Locate every blood parasite and identify its species.
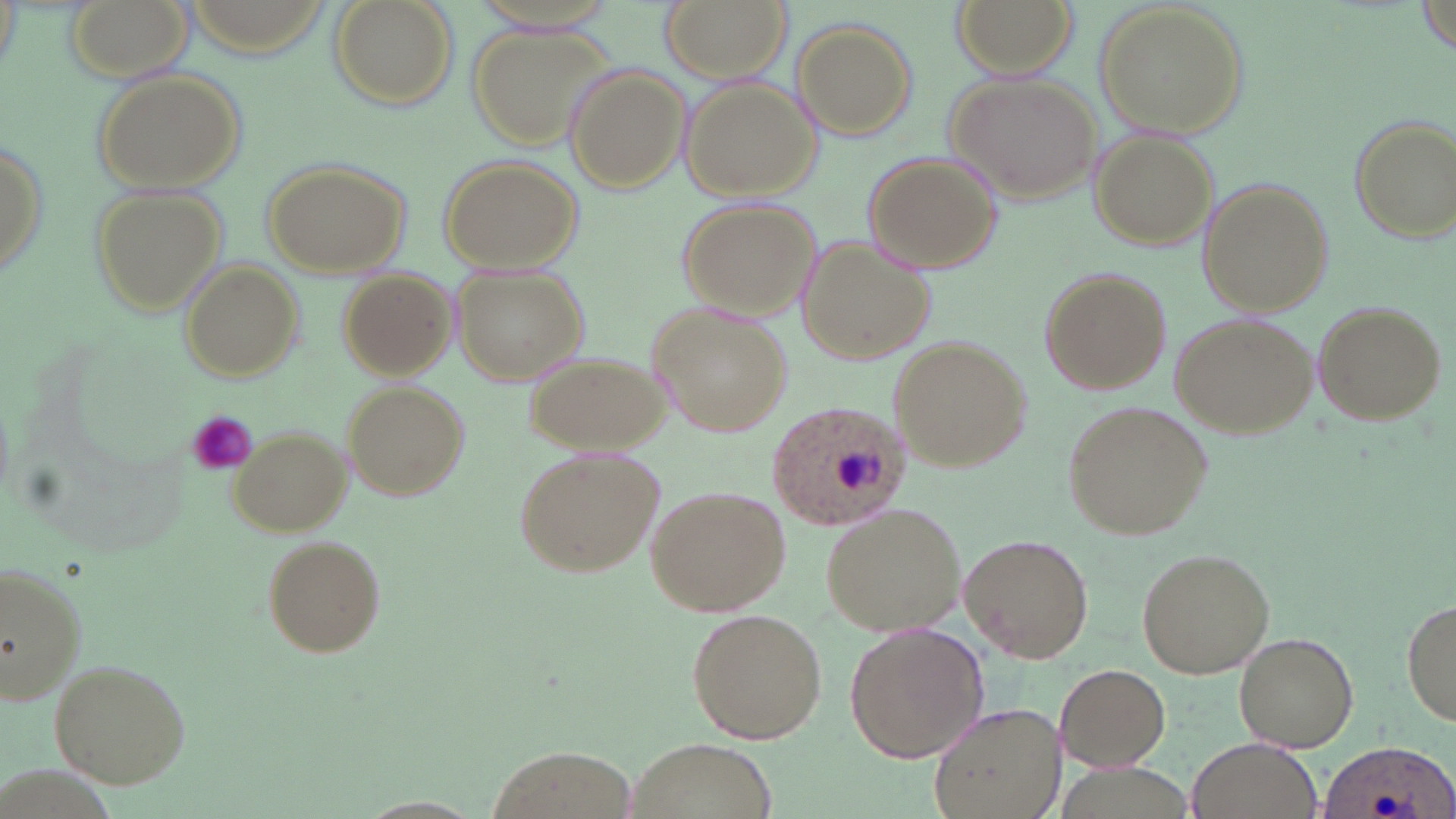
Approximate bounding boxes as (x1,y1)-(x2,y2) corner pairs in pixels.
Plasmodium ovale-infected red blood cells: (764,397)-(915,532), (1319,738)-(1456,819).
No Plasmodium falciparum, Plasmodium malariae, Plasmodium vivax, Babesia divergens, or Trypanosoma brucei observed.

Summary:
  - Platelet locations: (185,411)-(260,475)
  - Uninfected red blood cell locations: (65,0)-(193,80), (328,0)-(458,110), (660,0)-(788,81), (950,0)-(1075,77), (1096,0)-(1249,140), (1417,2)-(1455,59), (792,20)-(916,139), (470,23)-(616,152), (90,66)-(247,193), (565,66)-(690,194), (944,73)-(1102,205), (681,78)-(819,197), (1345,113)-(1455,244), (0,123)-(49,290), (1089,132)-(1221,250), (864,153)-(1003,275), (438,154)-(583,274), (263,158)-(409,277), (84,180)-(228,316), (1199,180)-(1331,317), (676,198)-(822,317), (796,235)-(935,366), (181,264)-(303,383), (452,264)-(590,386), (1039,266)-(1173,397), (336,270)-(455,380), (1311,299)-(1447,427), (647,302)-(793,437), (1172,310)-(1321,440), (890,333)-(1031,472), (522,348)-(670,454), (342,381)-(469,502), (1065,398)-(1213,541), (228,426)-(352,536), (515,443)-(664,578), (644,486)-(790,617), (820,503)-(966,638), (961,532)-(1096,664), (262,535)-(387,658), (1136,547)-(1276,680), (0,558)-(91,707), (1400,598)-(1456,729), (686,608)-(827,744), (845,620)-(989,764), (1235,631)-(1361,751), (45,656)-(192,787), (1056,662)-(1171,771), (928,701)-(1065,819), (1187,735)-(1320,819), (626,736)-(773,817), (491,746)-(631,819), (355,796)-(489,818)
  - Slide-level diagnosis: Plasmodium ovale
  - Image size: 1456×819 pixels
  - Field of view: single
  - Modality: light microscopy
  - Stain: May-Grünwald-Giemsa
  - Preparation: thin blood film
  - Magnification: 1000x